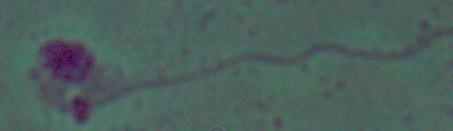
Summary:
  - Modality: photomicrograph
  - Identification: Leishmania
  - Magnification: 1000x